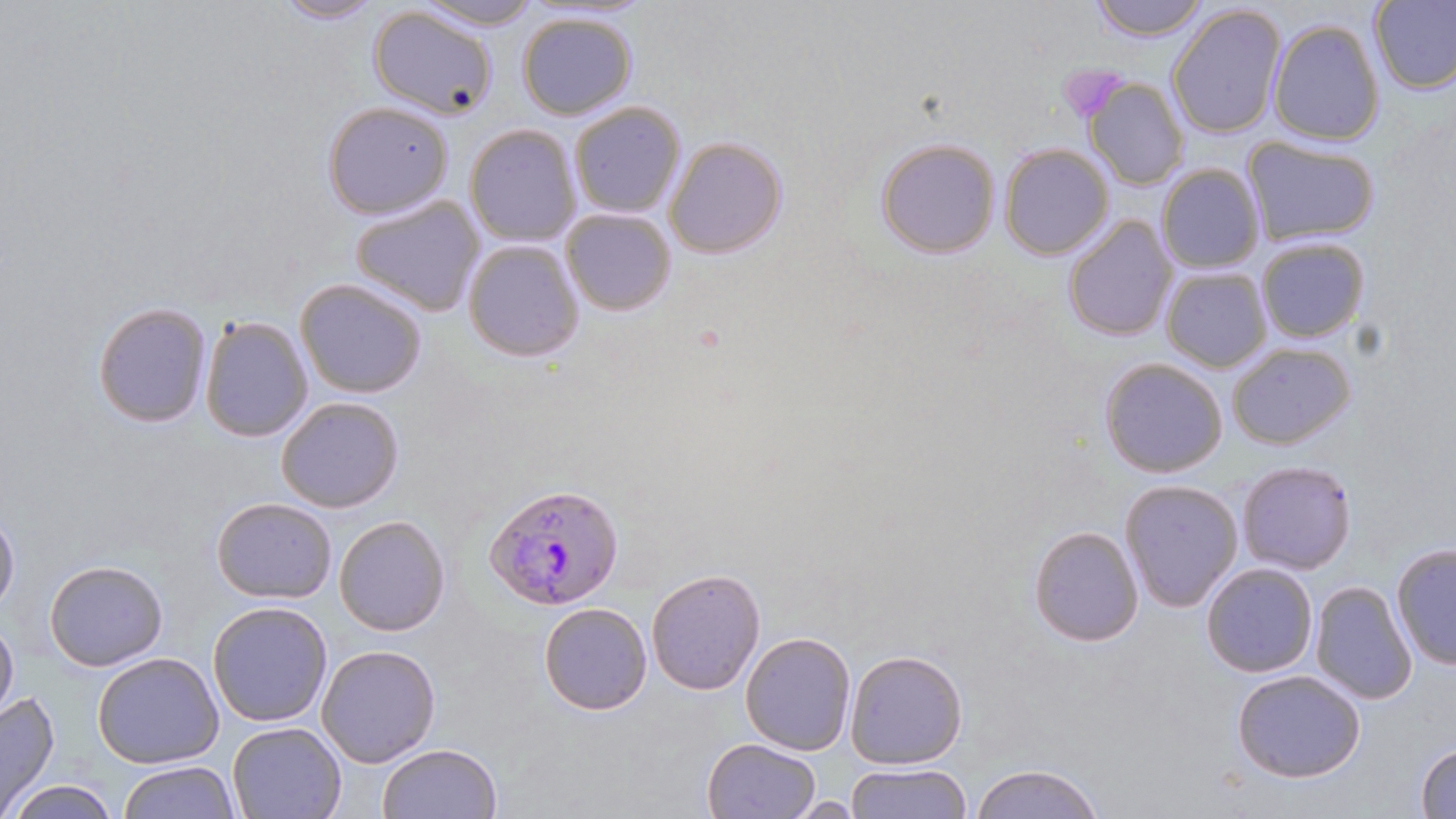 Approximate bounding boxes as (x1,y1)-(x2,y2) corner pairs in pixels. Uninfected red blood cell locations: (415,0)-(544,30), (1091,0)-(1208,40), (269,1)-(388,24), (1371,1)-(1456,95), (366,3)-(499,120), (1168,4)-(1288,140), (516,10)-(638,120), (1268,18)-(1384,146), (1083,76)-(1188,189), (321,100)-(455,217), (568,101)-(687,219), (465,124)-(582,247), (663,134)-(789,259), (876,135)-(1002,259), (1242,135)-(1380,247), (1000,144)-(1113,260), (1156,164)-(1265,273), (350,194)-(487,317), (561,207)-(678,315), (1063,213)-(1178,340), (1256,237)-(1370,345), (461,238)-(585,362), (1161,267)-(1272,372), (296,278)-(427,399), (93,302)-(212,427), (200,315)-(314,442), (1227,343)-(1355,451), (1098,356)-(1228,478), (276,396)-(404,513), (1236,459)-(1357,574), (1119,479)-(1243,614), (211,497)-(338,602), (0,509)-(19,614), (334,514)-(451,637), (1028,526)-(1143,647), (1390,541)-(1456,672), (43,559)-(168,670), (1200,562)-(1319,678), (647,568)-(766,695), (1310,581)-(1417,705), (208,602)-(333,726), (538,602)-(652,715), (0,619)-(18,719), (739,632)-(855,757), (315,643)-(441,768), (843,648)-(968,770), (93,653)-(223,768), (1230,670)-(1367,782), (0,689)-(60,815), (225,720)-(347,819), (700,737)-(822,819), (1413,741)-(1456,817), (376,743)-(503,819), (119,761)-(239,817), (844,763)-(972,819), (968,763)-(1107,819), (8,778)-(120,819), (787,795)-(866,816). Platelet locations: (1060,64)-(1128,120). Plasmodium falciparum-infected red blood cell locations: (486,483)-(625,610). Slide-level diagnosis: Plasmodium falciparum. Captured at 1000x magnification. Single field of view. Optical microscopy. May-Grünwald-Giemsa stain. Image is 1456×819 pixels. Thin blood film.